Classify this cell by malaria status.
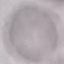

It is uninfected.

preparation = thin blood smear
image type = automatically extracted cell patch, resized to 64 × 64 pixels
stain = Giemsa
capture = smartphone camera at the microscope eyepiece